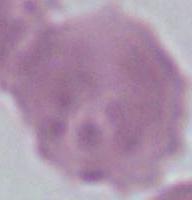

{
  "identification": "red blood cell",
  "magnification": "1000x",
  "modality": "photomicrograph"
}